Locate leukocytes (white blood cells).
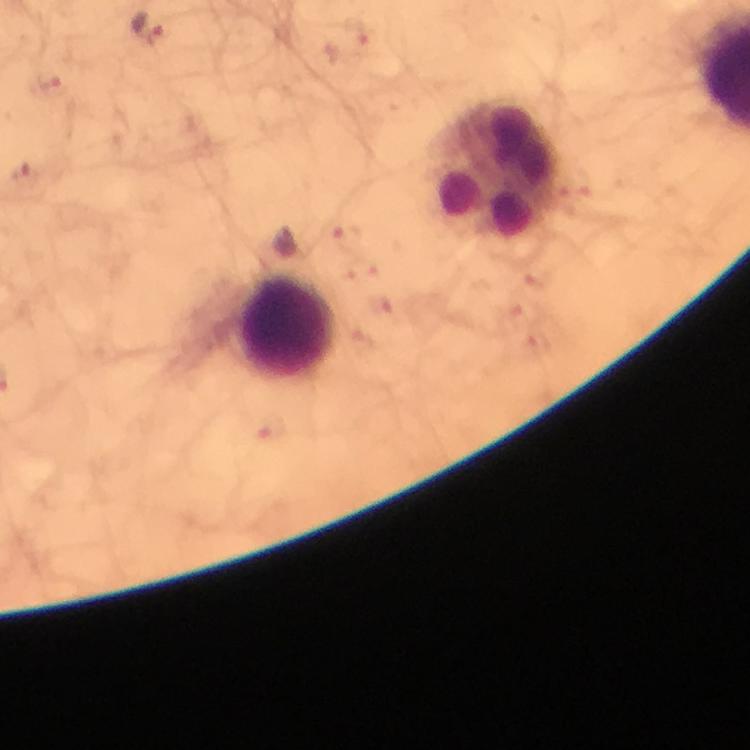

Approximate centers as {x, y} in pixels.
Leukocytes: {493, 170}, {286, 326}.

Malaria parasite locations: {146, 30}, {362, 33}, {49, 86}, {24, 174}, {345, 234}, {365, 276}, {541, 276}, {386, 306}, {513, 312}, {535, 343}, {275, 432}. Smartphone photograph taken through a microscope. Image is 750×750 pixels. At 100x magnification. From a malaria diagnostic workup. Immersion oil applied. Thick smear. Giemsa-stained preparation. Cropped region of a single field of view.